Name the blood parasite species.
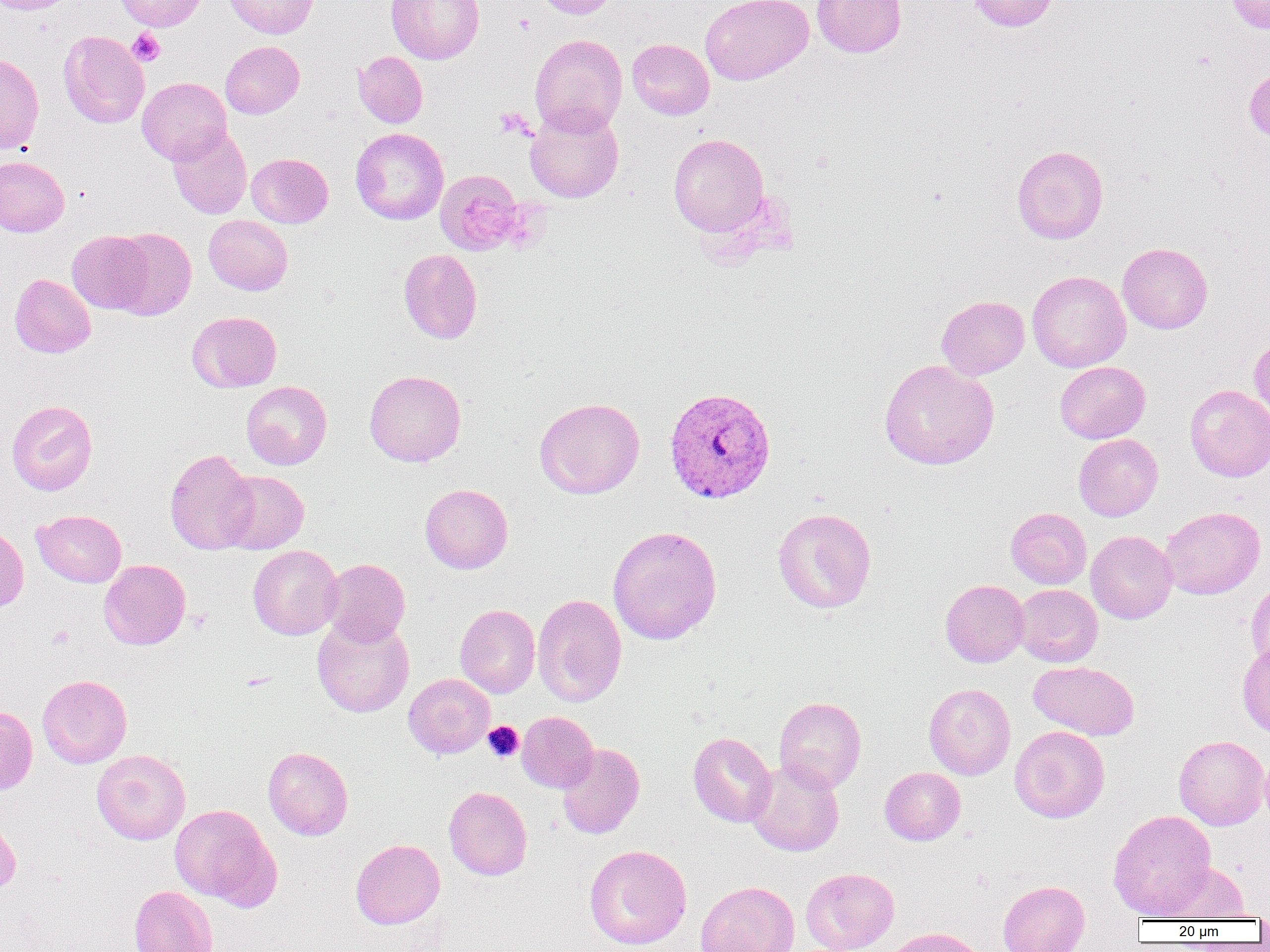
Plasmodium vivax.

Approximate bounding boxes as [x1, y1, x2, y2] in pixels. Plasmodium vivax-infected red blood cell locations: [664, 387, 776, 504]. Platelet locations: [128, 28, 166, 66], [495, 108, 534, 140], [483, 721, 523, 762]. Uninfected red blood cell locations: [0, 0, 80, 14], [114, 0, 206, 31], [224, 0, 318, 38], [386, 0, 484, 64], [534, 0, 619, 19], [701, 0, 814, 85], [811, 0, 906, 58], [966, 0, 1058, 31], [1225, 0, 1270, 34], [59, 31, 149, 128], [529, 34, 627, 136], [627, 38, 714, 120], [220, 41, 304, 118], [354, 51, 428, 128], [0, 52, 44, 153], [1244, 63, 1270, 143], [137, 77, 231, 165], [525, 105, 624, 203], [167, 125, 252, 219], [350, 127, 449, 225], [668, 133, 770, 237], [1012, 145, 1108, 244], [246, 153, 333, 228], [0, 156, 69, 236], [434, 169, 524, 255], [204, 215, 293, 295], [110, 227, 197, 320], [67, 230, 155, 314], [1117, 242, 1213, 333], [398, 249, 482, 344], [1027, 270, 1130, 372], [10, 273, 96, 358], [936, 295, 1029, 379], [186, 311, 282, 392], [1249, 335, 1270, 420], [879, 359, 999, 470], [1055, 361, 1150, 443], [364, 370, 466, 467], [241, 381, 332, 470], [1185, 384, 1270, 482], [534, 397, 645, 499], [6, 399, 98, 496], [1074, 434, 1163, 520], [165, 449, 258, 554], [220, 470, 308, 554], [420, 483, 513, 574], [1160, 506, 1265, 599], [773, 507, 876, 614], [1006, 507, 1091, 589], [32, 509, 126, 587], [0, 525, 29, 612], [607, 526, 722, 644], [1086, 530, 1177, 623], [248, 545, 343, 640], [321, 558, 410, 646], [99, 559, 190, 650], [1246, 578, 1270, 671], [940, 579, 1028, 667], [1013, 584, 1102, 667], [532, 593, 627, 707], [454, 604, 540, 698], [312, 615, 414, 717], [1237, 642, 1270, 739], [1028, 661, 1139, 740], [37, 674, 132, 768], [404, 674, 495, 758], [924, 683, 1015, 780], [774, 696, 866, 792], [0, 705, 38, 795], [517, 711, 599, 792], [1010, 725, 1110, 823], [688, 732, 776, 827], [1173, 735, 1269, 830], [557, 743, 644, 839], [1259, 746, 1270, 834], [263, 747, 353, 840], [91, 749, 190, 844], [746, 759, 844, 856], [880, 767, 966, 845], [443, 786, 532, 880], [170, 803, 280, 909], [1108, 809, 1217, 919], [0, 814, 21, 895], [351, 838, 445, 929], [584, 844, 692, 950], [1156, 862, 1249, 921], [801, 867, 899, 952], [696, 880, 800, 951], [998, 880, 1089, 952], [129, 885, 218, 952], [884, 927, 988, 952]. Thin blood film. Captured at 1000x magnification. Image is 1270×952 pixels. Optical microscopy. Single field of view.